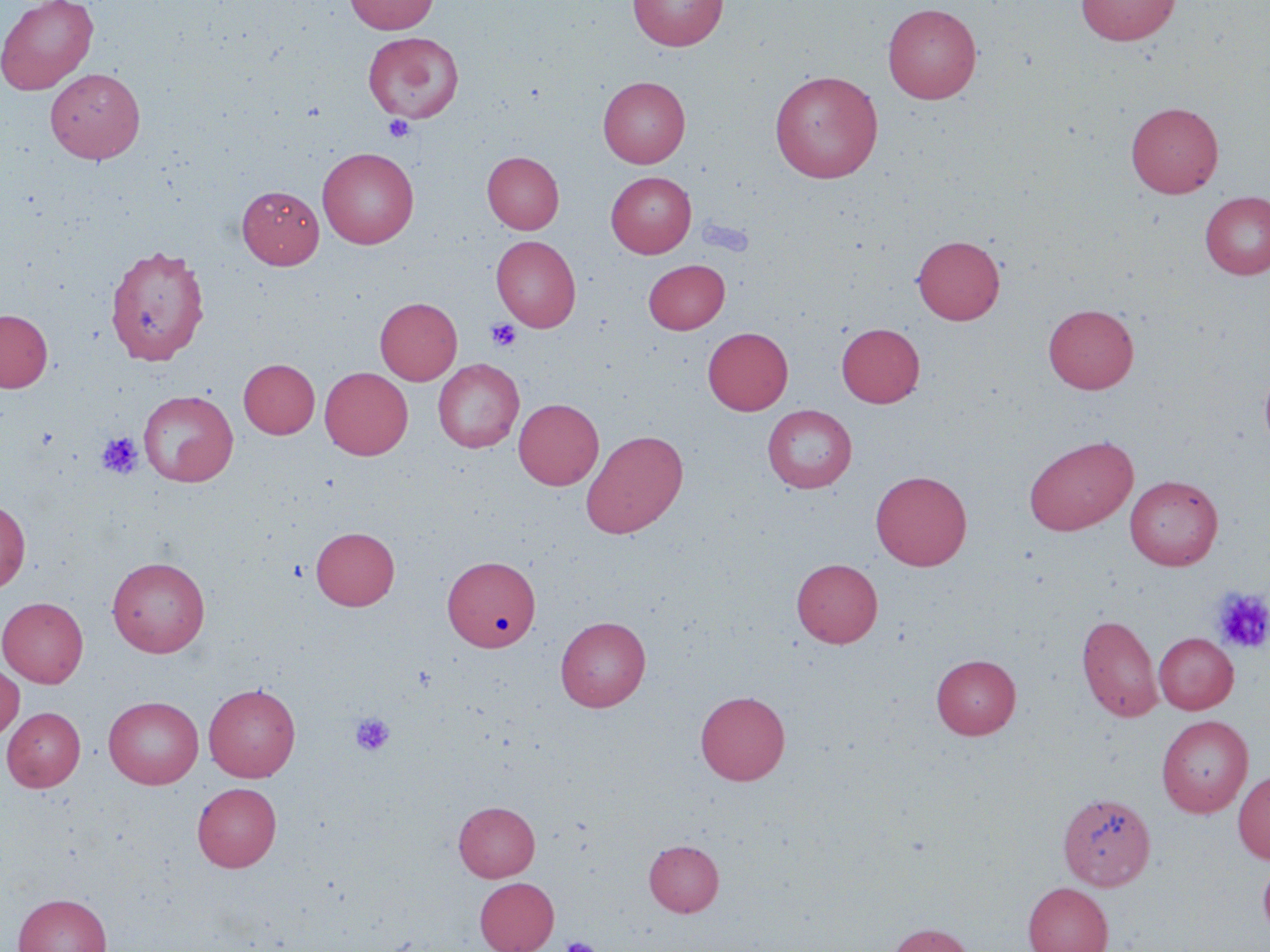

Approximate bounding boxes as [x1, y1, x2, y2] in pixels. Uninfected red blood cell locations: [0, 0, 98, 95], [344, 0, 438, 34], [628, 0, 727, 51], [1075, 0, 1180, 45], [882, 3, 982, 103], [362, 32, 464, 123], [45, 68, 145, 164], [769, 70, 884, 183], [598, 76, 690, 167], [1125, 102, 1223, 198], [317, 147, 419, 249], [482, 151, 563, 234], [607, 172, 696, 257], [237, 185, 324, 268], [1200, 191, 1270, 279], [491, 235, 581, 332], [912, 235, 1004, 324], [104, 244, 210, 365], [643, 259, 729, 333], [375, 297, 462, 384], [1043, 303, 1139, 394], [0, 309, 52, 392], [837, 322, 925, 407], [703, 327, 793, 415], [239, 358, 319, 439], [433, 359, 524, 452], [1259, 362, 1270, 454], [320, 367, 413, 459], [138, 390, 238, 486], [513, 398, 604, 490], [762, 405, 856, 493], [581, 429, 688, 538], [1023, 435, 1138, 536], [870, 470, 972, 570], [1125, 475, 1222, 570], [0, 500, 30, 593], [311, 526, 399, 610], [442, 555, 540, 652], [107, 556, 210, 657], [791, 558, 883, 647], [0, 597, 88, 687], [1077, 614, 1163, 722], [555, 616, 651, 711], [1154, 633, 1238, 714], [931, 654, 1021, 739], [0, 663, 24, 741], [204, 684, 300, 782], [695, 690, 790, 785], [104, 696, 203, 789], [2, 707, 85, 791], [1156, 715, 1252, 817], [1233, 770, 1270, 864], [192, 782, 282, 872], [1061, 797, 1160, 898], [454, 801, 540, 881], [644, 839, 724, 916], [1258, 856, 1270, 941], [474, 877, 558, 952], [1022, 882, 1113, 952], [14, 893, 111, 952], [886, 922, 974, 952]. Platelet locations: [383, 115, 414, 142], [486, 318, 522, 351], [97, 432, 144, 479], [1212, 588, 1270, 654], [350, 712, 395, 757], [561, 936, 600, 952]. Slide-level diagnosis: no evidence of blood parasites. Image is 1270×952 pixels. Thin blood film. Captured at 1000x magnification. One field of a larger specimen. Light microscopy. May-Grünwald-Giemsa stain.